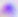 Toxoplasma gondii is shown. 400x magnification. Photomicrograph.